Name the blood parasite species.
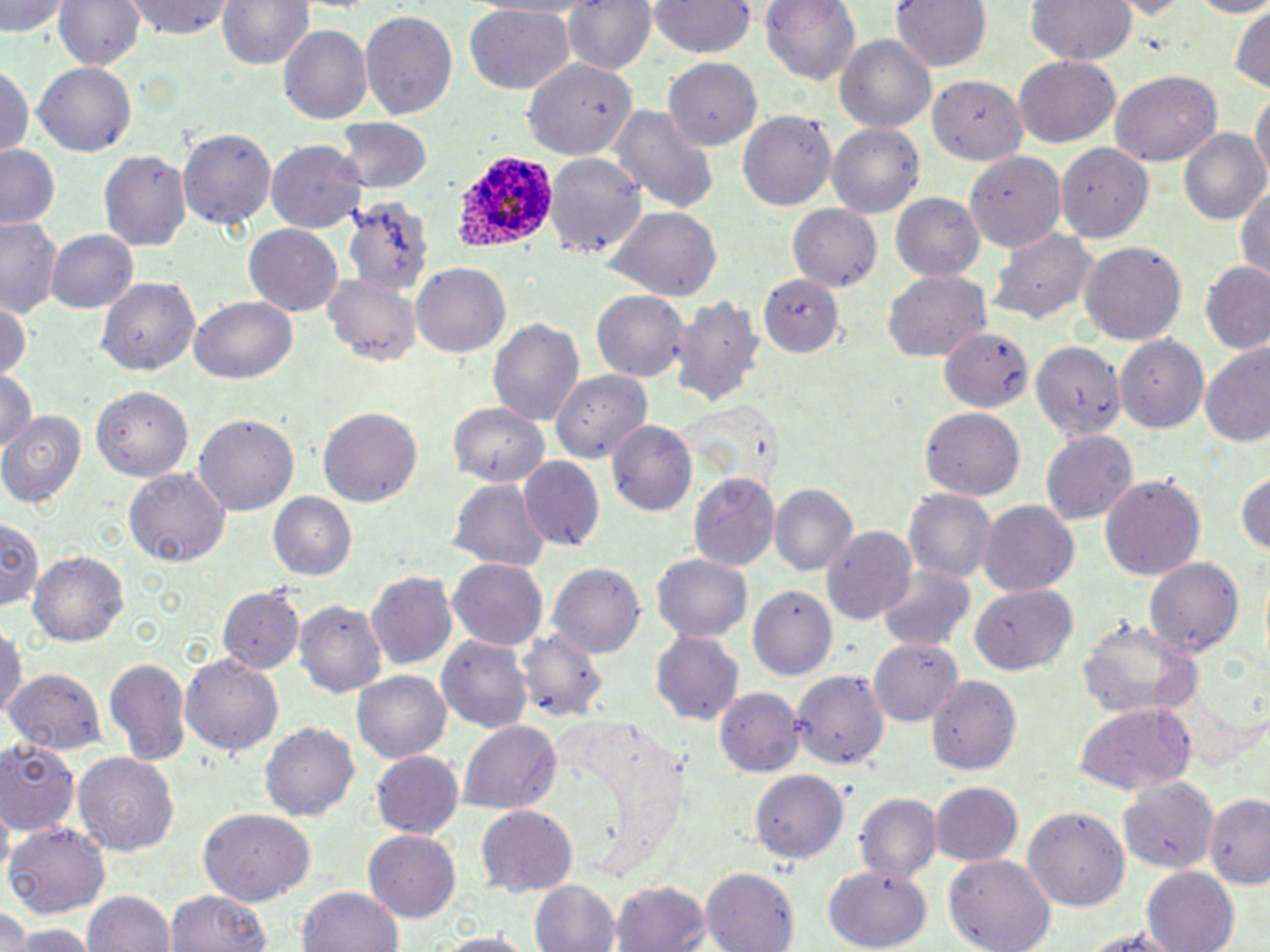
Plasmodium ovale.

Approximate bounding boxes as (x1,y1)-(x2,y2) corner pairs in pixels. Plasmodium ovale-infected red blood cell locations: (452,149)-(559,256). Uninfected red blood cell locations: (2,0)-(68,39), (53,0)-(144,71), (127,0)-(235,41), (220,0)-(312,71), (563,0)-(657,78), (760,0)-(862,86), (891,0)-(991,72), (1023,0)-(1138,66), (1182,0)-(1270,18), (650,1)-(754,58), (465,3)-(574,95), (1229,3)-(1269,89), (359,8)-(458,119), (279,25)-(372,125), (835,34)-(937,135), (520,55)-(636,158), (1013,57)-(1121,147), (664,60)-(761,148), (0,65)-(33,160), (34,65)-(136,155), (1109,71)-(1221,164), (930,77)-(1025,166), (1251,91)-(1269,188), (605,105)-(720,214), (739,110)-(836,211), (336,117)-(432,192), (828,122)-(924,221), (1180,127)-(1268,223), (178,128)-(276,231), (265,140)-(366,235), (1055,143)-(1151,242), (0,146)-(59,230), (101,150)-(191,251), (960,151)-(1066,252), (547,156)-(646,260), (1235,181)-(1270,280), (344,191)-(434,295), (892,194)-(986,281), (787,204)-(881,292), (603,205)-(722,300), (1,217)-(63,319), (243,221)-(343,314), (988,228)-(1100,327), (47,230)-(136,314), (1080,241)-(1186,347), (413,263)-(513,358), (1200,264)-(1270,354), (885,270)-(993,363), (323,274)-(420,366), (757,274)-(845,358), (99,277)-(200,376), (591,290)-(688,381), (671,294)-(764,409), (192,295)-(297,384), (0,300)-(30,386), (487,316)-(586,429), (939,327)-(1033,413), (1117,335)-(1208,427), (1031,340)-(1123,443), (1200,343)-(1270,449), (0,368)-(38,453), (550,368)-(653,465), (91,386)-(192,479), (449,402)-(551,486), (319,407)-(422,509), (923,409)-(1024,501), (0,410)-(86,509), (194,414)-(297,516), (609,419)-(699,517), (1040,430)-(1137,523), (519,458)-(605,552), (126,467)-(229,567), (1235,470)-(1270,557), (688,474)-(778,570), (1099,474)-(1205,579), (450,476)-(549,569), (770,486)-(856,578), (902,488)-(997,584), (267,492)-(357,580), (977,501)-(1079,597), (0,517)-(45,614), (822,526)-(918,625), (29,550)-(130,649), (653,554)-(752,642), (450,557)-(548,650), (1146,557)-(1247,658), (549,563)-(645,659), (875,564)-(976,651), (367,570)-(459,670), (972,583)-(1077,678), (219,584)-(303,674), (746,585)-(836,679), (295,600)-(387,696), (1078,614)-(1202,719), (0,626)-(26,721), (525,628)-(607,723), (437,631)-(533,730), (653,632)-(744,725), (868,638)-(963,728), (179,653)-(285,759), (105,656)-(192,768), (791,668)-(889,771), (3,669)-(105,758), (353,669)-(451,761), (927,675)-(1020,775), (715,686)-(803,776), (1072,701)-(1197,797), (261,720)-(359,827), (459,720)-(563,815), (0,737)-(80,835), (72,749)-(181,854), (372,750)-(465,838), (751,769)-(850,864), (1116,775)-(1221,875), (929,781)-(1022,868), (1203,793)-(1270,888), (854,794)-(941,884), (1024,804)-(1129,910), (476,805)-(577,894), (198,808)-(314,906), (5,822)-(111,916), (364,830)-(462,921), (945,854)-(1056,952), (826,866)-(934,949), (1142,866)-(1242,952), (702,868)-(800,952), (531,879)-(621,952), (611,879)-(712,952), (298,886)-(405,952), (83,889)-(176,952), (164,889)-(273,952), (0,908)-(31,951), (15,924)-(95,952), (1071,925)-(1192,949), (426,932)-(543,951). One field of a larger specimen. Image is 1270×952 pixels. Captured at 1000x magnification. May-Grünwald-Giemsa-stained preparation. Optical microscopy. Thin blood film.